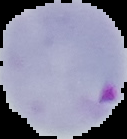
result = malaria parasites identified
image type = cell region segmented out of the field of view; surrounding area masked to black
preparation = thin blood film
image size = 127×139 pixels